State which parasite is depicted.
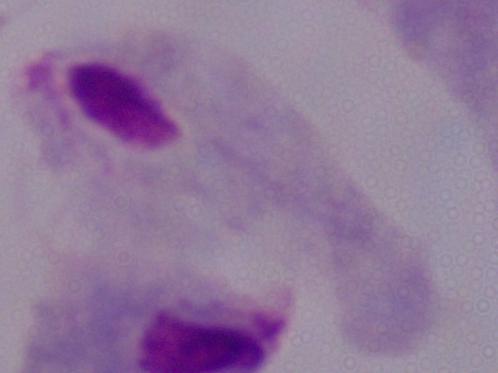

A trichomonad.

magnification = 1000x
modality = micrograph